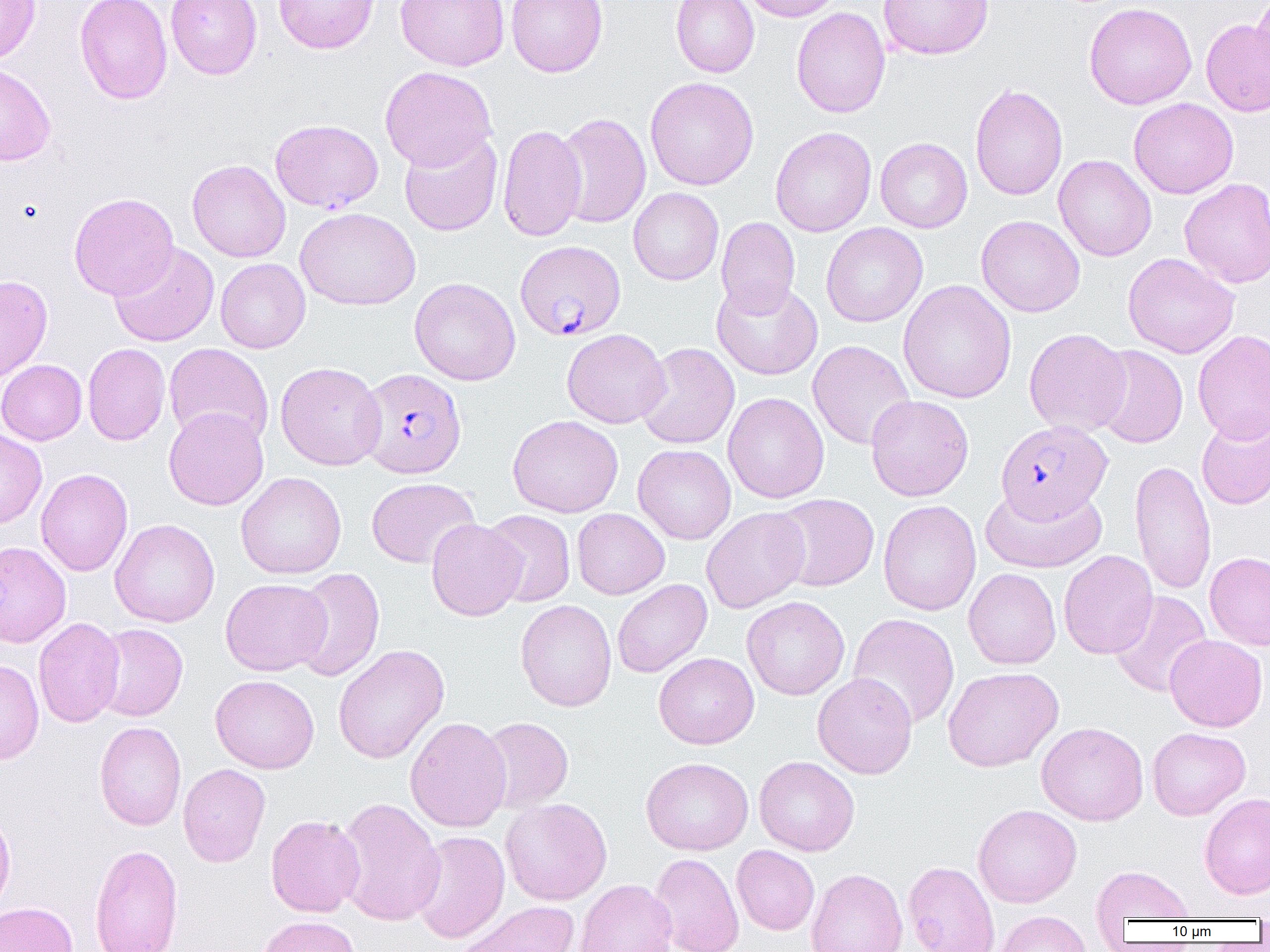
Summary:
  - Coordinate format: approximate bounding boxes as (x1, y1, x2, y2) in pixels
  - Plasmodium falciparum-infected red blood cell locations (subset): (515, 240, 626, 341), (356, 368, 467, 478), (997, 419, 1114, 522)
  - Uninfected red blood cell locations (subset): (0, 0, 41, 63), (74, 0, 173, 104), (165, 0, 262, 80), (274, 0, 379, 54), (395, 0, 510, 71), (506, 0, 608, 77), (671, 0, 760, 78), (737, 0, 844, 22), (877, 0, 994, 60), (1251, 0, 1270, 85), (1083, 2, 1197, 110), (791, 7, 890, 119), (1201, 19, 1270, 116), (0, 63, 56, 166), (379, 66, 497, 171), (645, 77, 759, 190), (970, 84, 1068, 200), (1129, 98, 1239, 199), (554, 113, 651, 229), (497, 124, 587, 242), (770, 127, 876, 237), (399, 131, 502, 236), (875, 137, 973, 233), (1053, 154, 1156, 261), (187, 159, 290, 262), (1179, 178, 1270, 288), (628, 187, 724, 285), (69, 192, 179, 300), (295, 207, 421, 310), (976, 215, 1085, 317), (716, 217, 800, 317), (821, 222, 927, 327), (109, 242, 219, 347), (1122, 252, 1240, 358), (215, 258, 311, 353), (0, 275, 53, 383), (409, 277, 521, 386), (711, 278, 824, 380), (897, 280, 1017, 404), (1024, 327, 1132, 437), (562, 328, 670, 428), (1193, 330, 1270, 444), (807, 340, 916, 450), (83, 343, 170, 445), (164, 343, 274, 447), (636, 343, 740, 449), (1092, 345, 1188, 449), (0, 359, 87, 445), (275, 361, 386, 470), (723, 392, 829, 503), (866, 394, 973, 501), (163, 406, 268, 510), (1196, 412, 1270, 510), (507, 414, 623, 518), (0, 428, 47, 529), (633, 444, 736, 544), (1129, 459, 1216, 596), (36, 468, 133, 576), (236, 472, 346, 579), (366, 477, 479, 568), (980, 481, 1107, 573), (772, 493, 880, 592), (878, 499, 981, 616), (701, 507, 811, 613), (572, 508, 669, 599), (482, 510, 576, 607), (110, 518, 220, 627), (426, 518, 526, 621), (0, 541, 71, 648), (1058, 550, 1158, 659), (1204, 552, 1270, 651), (291, 567, 385, 682), (964, 568, 1061, 669), (220, 578, 332, 676), (612, 579, 712, 678), (1109, 591, 1213, 697), (741, 596, 850, 700), (515, 599, 617, 711), (847, 613, 960, 729), (33, 617, 125, 728), (93, 623, 188, 721), (1165, 634, 1267, 731), (333, 643, 449, 764), (653, 652, 759, 749), (0, 658, 44, 765), (942, 666, 1063, 772), (812, 672, 917, 778), (210, 675, 319, 773), (405, 716, 512, 832), (480, 717, 574, 813), (94, 721, 187, 830), (1036, 721, 1148, 825), (1147, 727, 1250, 820), (641, 756, 753, 855), (754, 756, 860, 856), (178, 763, 271, 867), (1199, 792, 1270, 900), (335, 797, 445, 926), (500, 797, 612, 905), (973, 804, 1082, 908), (0, 808, 16, 919), (266, 815, 365, 917), (410, 830, 510, 943), (89, 844, 184, 952), (732, 845, 820, 935), (650, 852, 744, 952), (903, 860, 999, 952), (1091, 865, 1196, 922), (805, 868, 908, 952), (575, 879, 677, 952), (0, 901, 79, 952), (456, 901, 580, 952), (994, 910, 1092, 952), (256, 915, 361, 952)
  - Slide-level diagnosis: Plasmodium falciparum
  - Image size: 1270×952 pixels
  - Field of view: single
  - Modality: light microscopy
  - Preparation: thin blood film
  - Magnification: 1000x